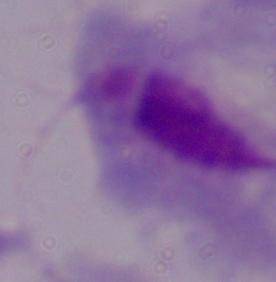

{
  "modality": "photomicrograph",
  "identification": "trichomonad",
  "magnification": "1000x"
}